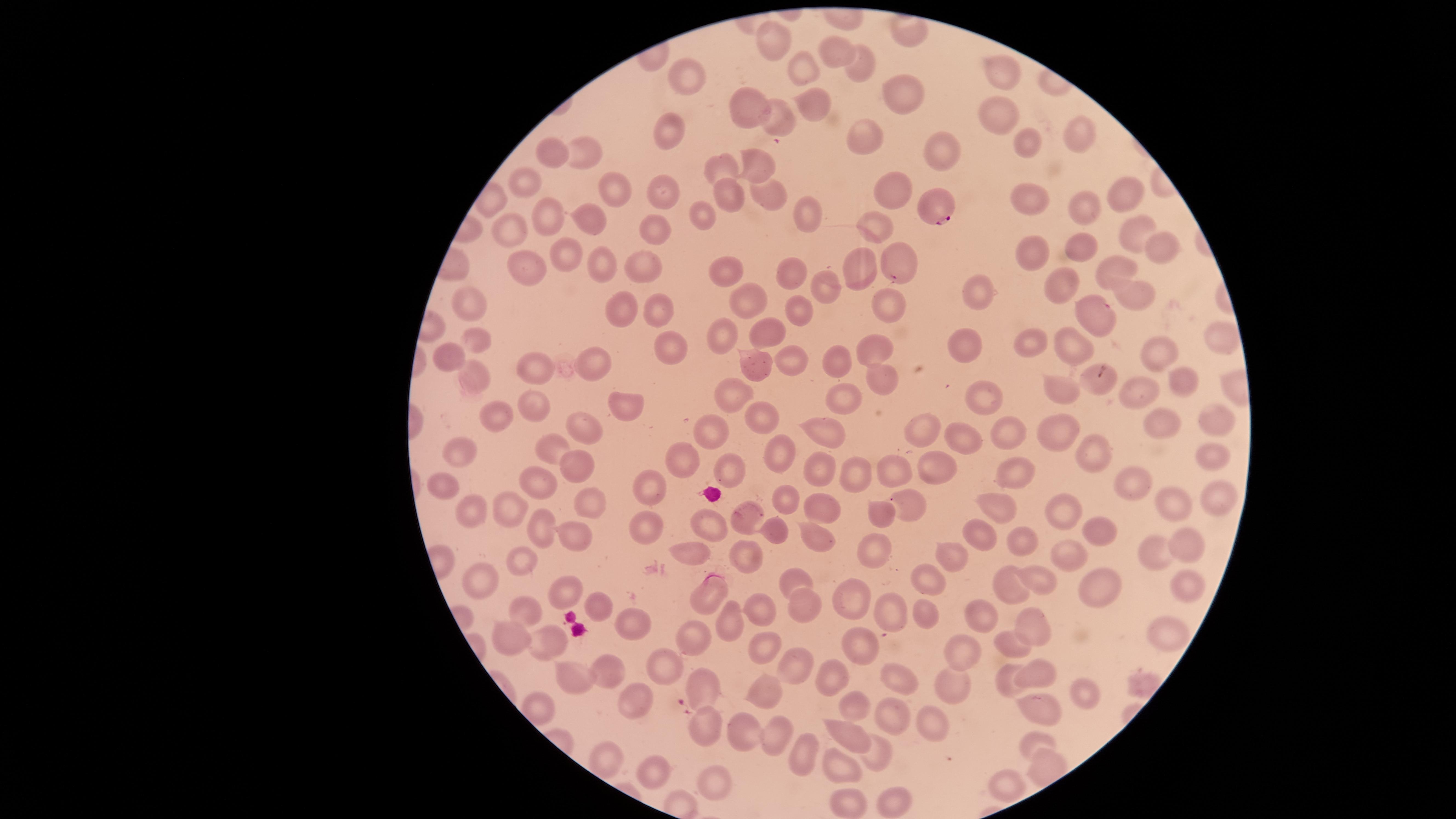 Approximate marker points as [x, y] in pixels. Parasitized red blood cells: [935, 204]. Uninfected red blood cells: [910, 36], [769, 40], [832, 50], [999, 64], [857, 66], [804, 72], [683, 73], [906, 92], [750, 101], [809, 105], [1000, 115], [1084, 131], [669, 132], [859, 139], [944, 146], [1025, 146], [587, 148], [552, 151], [756, 159], [724, 166], [527, 181], [661, 186], [609, 189], [891, 189], [1117, 190], [765, 195], [729, 196], [1023, 199], [1078, 204], [705, 214], [552, 215], [810, 216], [590, 219], [869, 228], [1126, 228], [656, 229], [513, 230], [1151, 246], [1085, 250], [1030, 253], [901, 259], [569, 261], [863, 261], [606, 262], [640, 264], [733, 266], [523, 267], [1111, 270], [794, 271], [1065, 283], [1135, 287], [976, 289], [829, 291], [469, 301], [746, 302], [886, 302], [621, 306], [798, 309], [664, 310], [1097, 312], [768, 332], [726, 335], [479, 338], [1215, 338], [1028, 341], [1073, 345], [966, 346], [1157, 347], [669, 348], [877, 351], [448, 353], [835, 359], [751, 363], [789, 363], [598, 364], [533, 369], [886, 371], [476, 373], [1102, 378], [1180, 383], [1064, 388], [735, 390], [982, 392], [841, 393], [1138, 395], [537, 409], [621, 409], [759, 412], [491, 414], [1160, 418], [1215, 419], [710, 425], [1057, 428], [582, 429], [916, 429], [824, 432], [1006, 433], [967, 439], [550, 446], [463, 450], [1208, 454], [1095, 456], [772, 457], [684, 461], [580, 463], [930, 463], [821, 466], [726, 468], [855, 468], [1009, 469], [891, 473], [536, 480], [1138, 482], [448, 485], [648, 486], [1216, 495], [589, 499], [1165, 499], [782, 500], [1003, 504], [907, 505], [509, 508], [826, 508], [1063, 513], [477, 516], [743, 518], [881, 518], [707, 525], [541, 527], [642, 527], [579, 529], [775, 529], [1096, 531], [981, 535], [811, 539], [1185, 540], [1029, 542], [872, 550], [948, 553], [689, 554], [1155, 555], [744, 558], [1068, 562], [529, 571], [796, 576], [931, 577], [1043, 578], [1184, 579], [482, 582], [1004, 583], [1105, 583], [561, 588], [709, 591], [846, 599], [594, 601], [804, 602], [754, 604], [524, 607], [926, 612], [891, 614], [979, 615], [1034, 618], [732, 620], [1167, 631], [628, 633], [862, 640], [512, 641], [692, 641], [760, 642], [1014, 642], [964, 648], [551, 649], [796, 664], [663, 667], [602, 671], [1031, 671], [900, 675], [570, 677], [832, 679], [955, 680], [1006, 683], [700, 684], [1083, 687], [765, 694], [536, 702], [631, 702], [850, 705], [1038, 711], [889, 714], [935, 717], [707, 721], [853, 731], [739, 732], [771, 732], [1035, 735], [797, 751], [871, 759], [613, 760], [1044, 764], [841, 767], [656, 771], [712, 781], [1006, 786], [896, 797], [849, 801]. One field of view of the specimen. Thin blood film. Giemsa-stained preparation. Presence: malaria parasites detected. Smartphone photograph through the microscope eyepiece. Circular visible region. Species: Plasmodium falciparum. Image is 1456×819 pixels.